Classify this cell by malaria status.
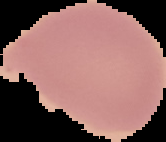
It is uninfected.

Segmented cell region on a black background. Image is 166×142 pixels. From a thin blood smear.